Evaluate for malaria.
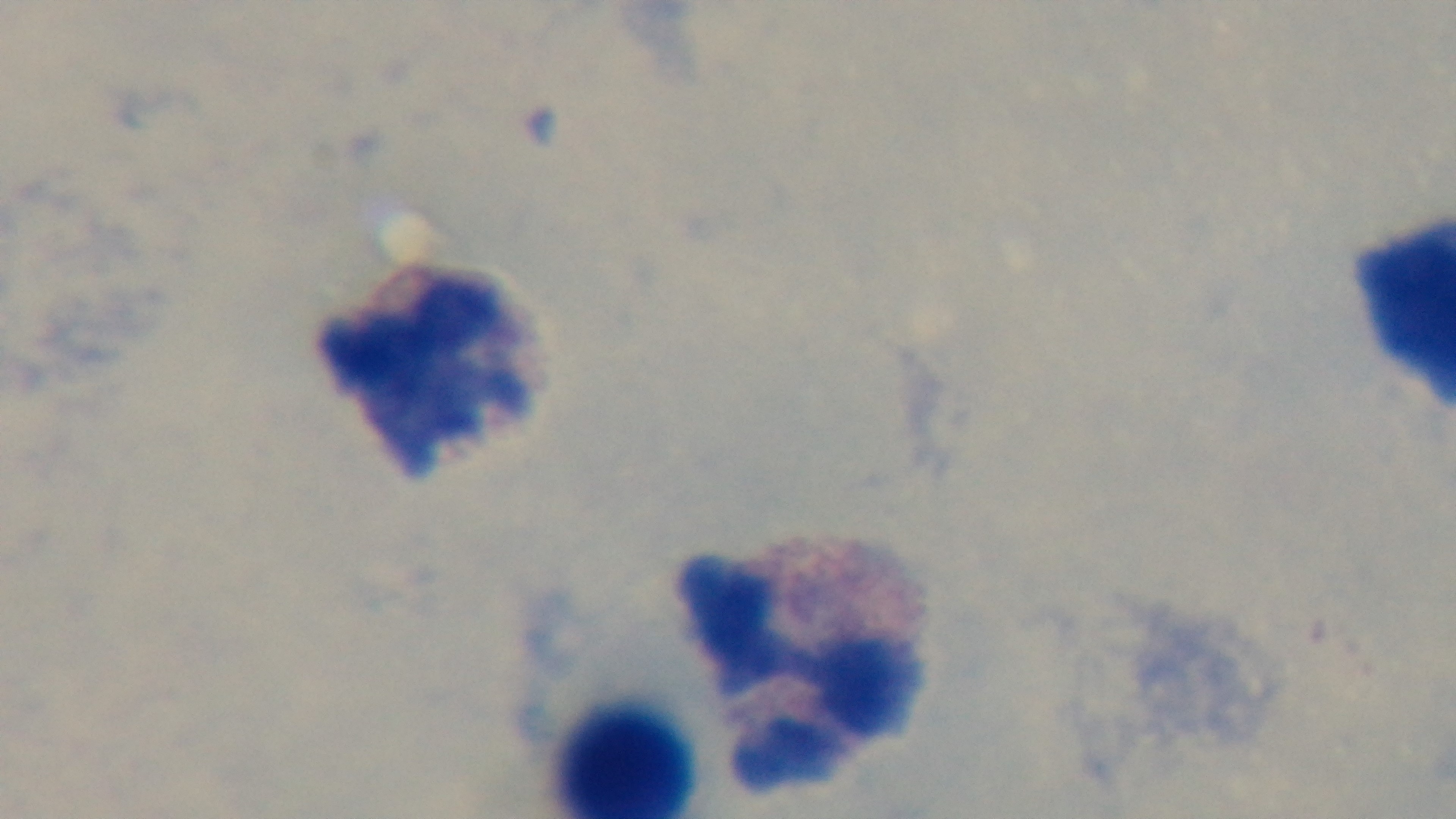

Uninfected.

Giemsa stain. One field from the slide. Preparation: thick blood film. Mounted 4K digital camera. Oil-immersion objective, 100x. Light microscopy.